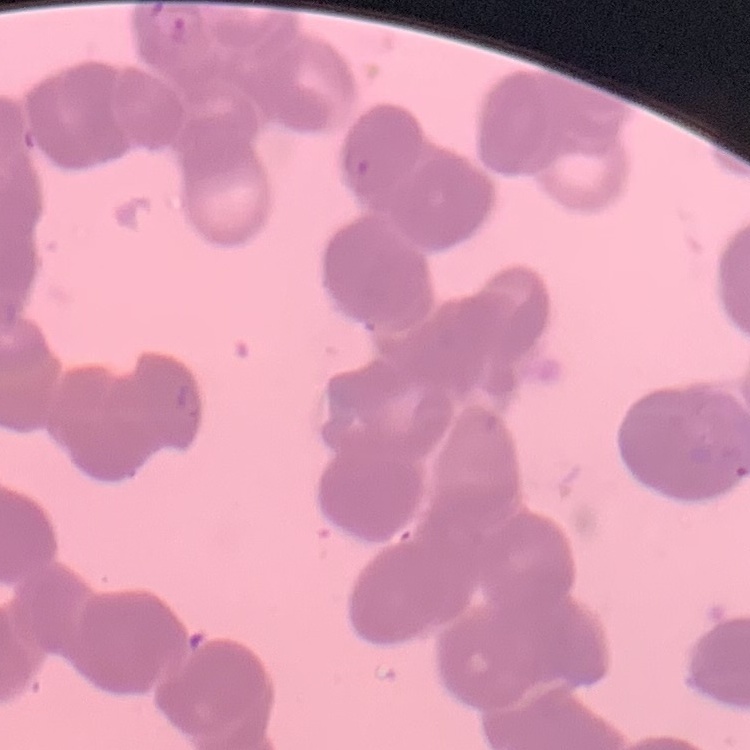
{
  "red_blood_cell_morphology": "rouleaux formation",
  "image_type": "one tile cut from a larger photomicrograph",
  "stain": "Field's or Giemsa",
  "preparation": "thin peripheral smear"
}